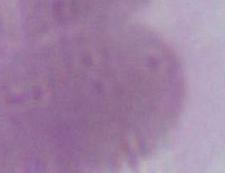

identification = red blood cell
modality = photomicrograph
magnification = 1000x